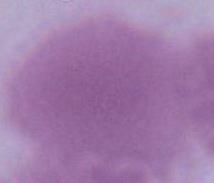
{
  "magnification": "1000x",
  "modality": "photomicrograph",
  "identification": "erythrocyte"
}